Report the malaria status of this cell.
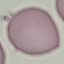

Uninfected.

Acquired by smartphone through the microscope eyepiece. Cell patch, automatically extracted from a larger field of view and resized to 64 × 64 pixels. Giemsa stain. Thin blood film.